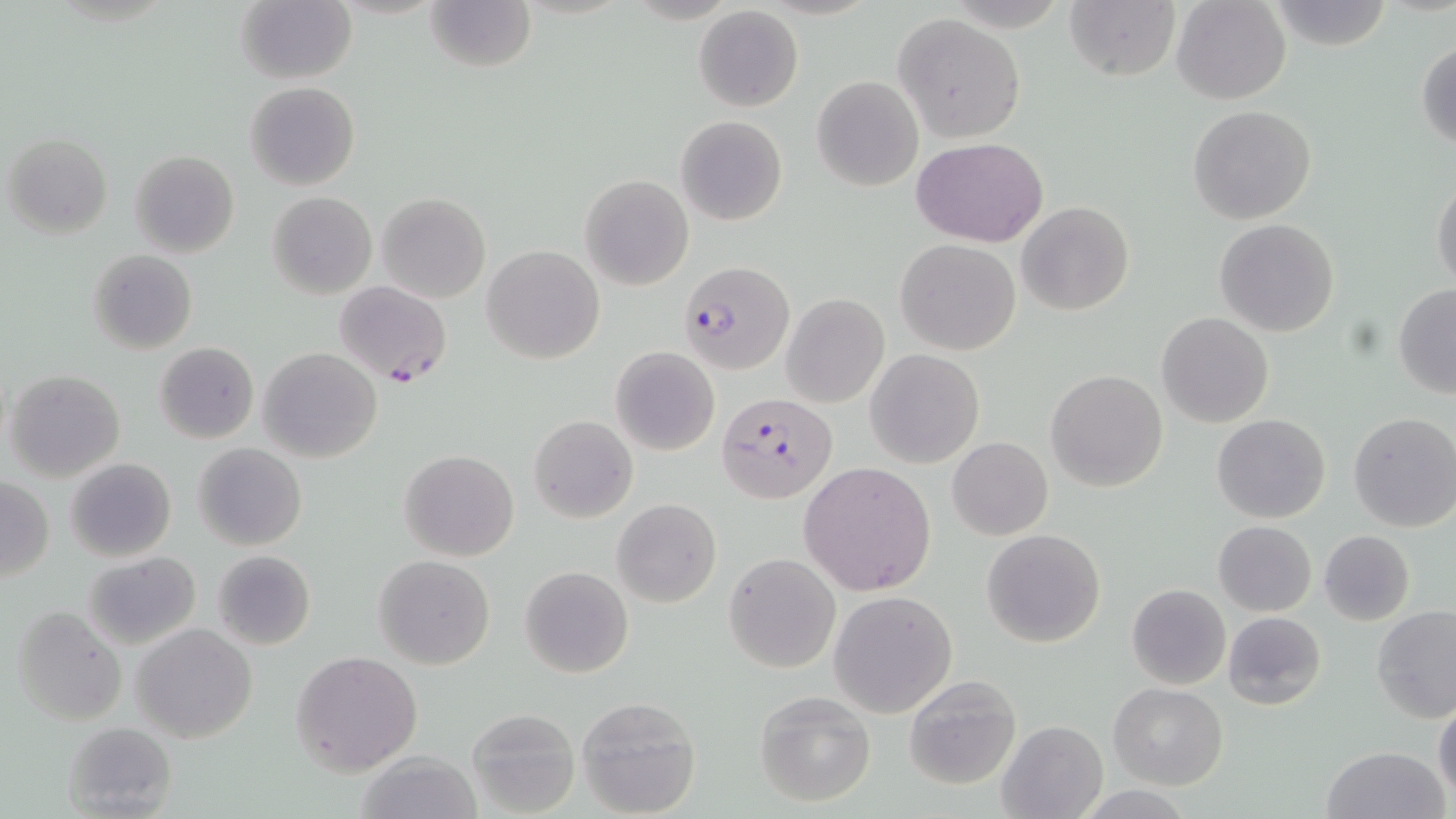

Summary:
  - Coordinate format: approximate bounding boxes as named x1/y1/x2/y2 corners in pixels
  - Uninfected red blood cell locations: (x1=426, y1=0, x2=535, y2=74), (x1=1062, y1=0, x2=1179, y2=81), (x1=1170, y1=0, x2=1291, y2=105), (x1=1264, y1=0, x2=1396, y2=50), (x1=236, y1=1, x2=355, y2=84), (x1=694, y1=6, x2=803, y2=113), (x1=892, y1=14, x2=1025, y2=141), (x1=1415, y1=39, x2=1456, y2=151), (x1=812, y1=75, x2=923, y2=191), (x1=245, y1=81, x2=360, y2=191), (x1=1188, y1=104, x2=1316, y2=224), (x1=676, y1=115, x2=787, y2=225), (x1=4, y1=134, x2=112, y2=239), (x1=911, y1=137, x2=1049, y2=246), (x1=130, y1=150, x2=239, y2=259), (x1=579, y1=173, x2=695, y2=290), (x1=1430, y1=176, x2=1455, y2=293), (x1=267, y1=192, x2=377, y2=300), (x1=377, y1=193, x2=490, y2=303), (x1=1017, y1=202, x2=1135, y2=316), (x1=1215, y1=219, x2=1339, y2=337), (x1=895, y1=239, x2=1021, y2=354), (x1=483, y1=245, x2=603, y2=364), (x1=88, y1=249, x2=197, y2=355), (x1=1393, y1=285, x2=1456, y2=396), (x1=781, y1=293, x2=889, y2=407), (x1=1156, y1=311, x2=1273, y2=427), (x1=154, y1=342, x2=259, y2=444), (x1=611, y1=346, x2=720, y2=456), (x1=259, y1=347, x2=382, y2=463), (x1=866, y1=349, x2=984, y2=467), (x1=5, y1=369, x2=125, y2=482), (x1=1045, y1=370, x2=1168, y2=492), (x1=1348, y1=412, x2=1456, y2=532), (x1=1212, y1=413, x2=1331, y2=523), (x1=528, y1=414, x2=638, y2=524), (x1=947, y1=437, x2=1053, y2=540), (x1=193, y1=443, x2=307, y2=551), (x1=398, y1=449, x2=519, y2=562), (x1=66, y1=457, x2=176, y2=562), (x1=799, y1=461, x2=936, y2=596), (x1=1, y1=477, x2=53, y2=582), (x1=612, y1=499, x2=721, y2=607), (x1=1213, y1=521, x2=1316, y2=616), (x1=981, y1=528, x2=1106, y2=648), (x1=1318, y1=530, x2=1416, y2=626), (x1=212, y1=549, x2=316, y2=649), (x1=82, y1=551, x2=202, y2=651), (x1=725, y1=553, x2=841, y2=673), (x1=373, y1=555, x2=496, y2=670), (x1=520, y1=565, x2=633, y2=678), (x1=1126, y1=584, x2=1231, y2=690), (x1=829, y1=590, x2=959, y2=719), (x1=11, y1=604, x2=125, y2=725), (x1=1372, y1=606, x2=1456, y2=724), (x1=1223, y1=612, x2=1327, y2=711), (x1=131, y1=623, x2=258, y2=745), (x1=290, y1=650, x2=423, y2=776), (x1=902, y1=672, x2=1022, y2=790), (x1=1107, y1=683, x2=1228, y2=790), (x1=753, y1=689, x2=876, y2=807), (x1=578, y1=697, x2=701, y2=818), (x1=1433, y1=698, x2=1456, y2=803), (x1=465, y1=707, x2=580, y2=817), (x1=62, y1=721, x2=177, y2=816), (x1=996, y1=721, x2=1107, y2=819), (x1=1321, y1=745, x2=1449, y2=819), (x1=356, y1=750, x2=483, y2=819)
  - Plasmodium falciparum-infected red blood cell locations: (x1=678, y1=261, x2=795, y2=373), (x1=333, y1=280, x2=453, y2=386), (x1=716, y1=391, x2=835, y2=502)
  - Slide-level diagnosis: Plasmodium falciparum
  - Preparation: thin blood smear
  - Field of view: single
  - Magnification: 1000x
  - Stain: May-Grünwald-Giemsa
  - Modality: light microscopy
  - Image size: 1456×819 pixels